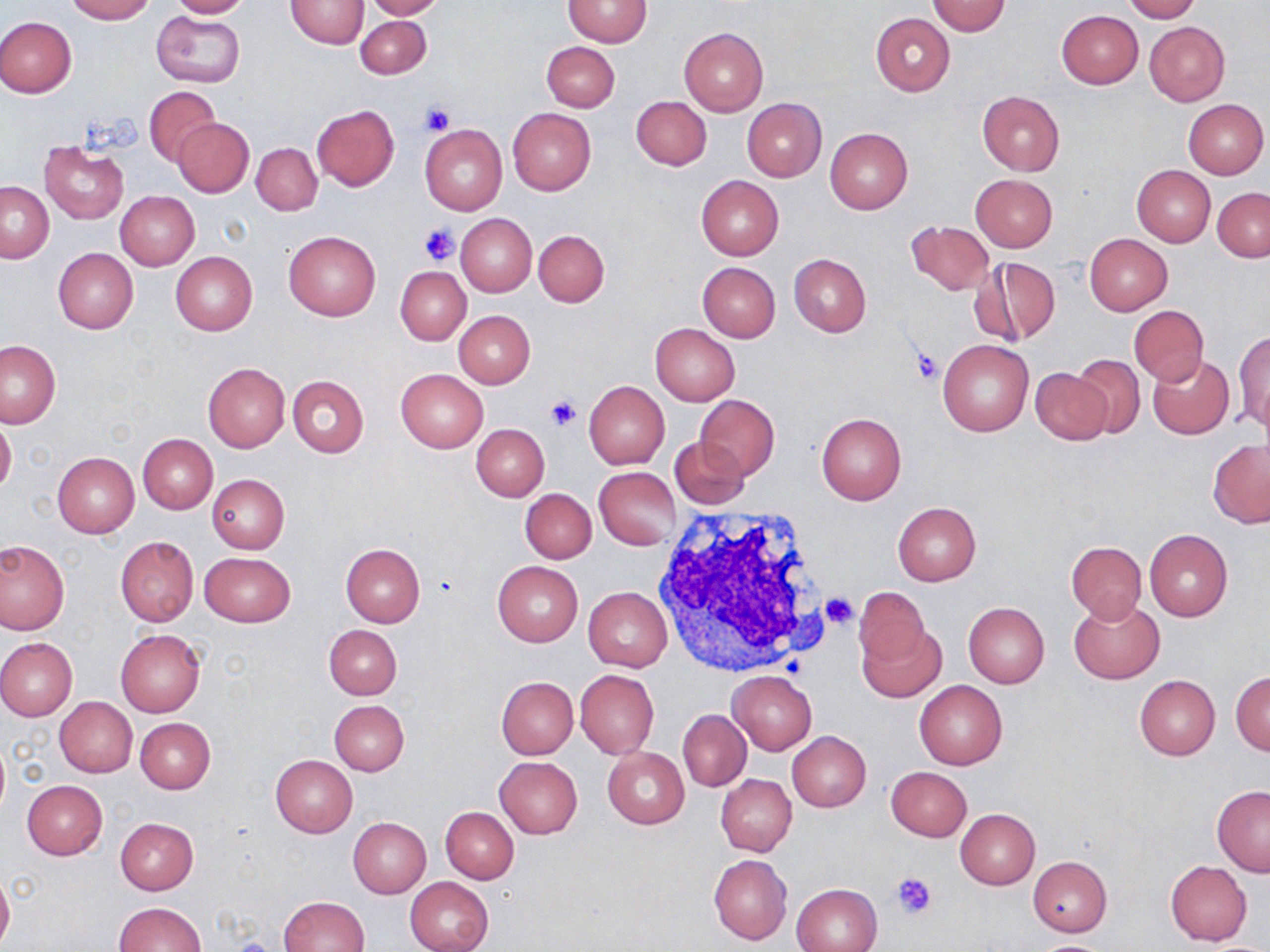

Approximate bounding boxes as [x1, y1, x2, y2] in pixels. Uninfected red blood cell locations: [65, 0, 154, 23], [167, 0, 254, 18], [286, 0, 368, 49], [362, 0, 445, 20], [562, 0, 653, 47], [1122, 0, 1201, 23], [926, 1, 1012, 37], [297, 5, 433, 65], [152, 11, 244, 88], [1055, 11, 1142, 89], [870, 13, 955, 96], [0, 16, 76, 98], [354, 16, 431, 79], [1145, 22, 1229, 105], [679, 27, 768, 116], [541, 41, 620, 112], [144, 88, 222, 167], [976, 90, 1065, 175], [631, 96, 711, 170], [741, 98, 826, 182], [1184, 100, 1268, 179], [312, 104, 399, 191], [508, 109, 595, 195], [174, 118, 253, 197], [420, 123, 507, 215], [825, 128, 913, 214], [39, 141, 129, 224], [252, 143, 322, 215], [1132, 165, 1215, 246], [971, 174, 1057, 252], [696, 175, 783, 260], [1, 182, 54, 262], [1213, 187, 1270, 261], [116, 191, 199, 270], [456, 214, 536, 295], [906, 220, 994, 296], [533, 229, 609, 307], [283, 231, 380, 321], [1084, 234, 1173, 315], [52, 247, 139, 334], [170, 251, 258, 335], [788, 254, 871, 337], [975, 257, 1061, 348], [697, 261, 781, 342], [395, 266, 471, 345], [1129, 307, 1209, 385], [454, 310, 536, 387], [650, 323, 740, 405], [1234, 330, 1270, 433], [938, 339, 1034, 437], [1, 340, 61, 429], [1071, 353, 1145, 438], [1148, 353, 1235, 439], [202, 363, 290, 452], [395, 368, 488, 452], [1030, 368, 1114, 445], [288, 375, 369, 457], [584, 380, 670, 469], [693, 394, 780, 480], [816, 412, 906, 504], [0, 416, 17, 497], [471, 424, 549, 501], [139, 435, 218, 513], [669, 436, 749, 509], [1208, 439, 1269, 527], [52, 452, 140, 538], [594, 467, 681, 549], [208, 474, 290, 553], [520, 488, 596, 564], [892, 501, 981, 584], [1145, 529, 1232, 620], [115, 537, 199, 626], [1, 541, 68, 635], [1067, 541, 1146, 622], [340, 543, 425, 627], [200, 552, 295, 628], [493, 562, 583, 645], [853, 585, 932, 668], [583, 586, 673, 672], [1068, 598, 1166, 684], [963, 601, 1049, 688], [859, 621, 945, 703], [323, 624, 401, 699], [116, 629, 205, 717], [0, 638, 77, 721], [575, 669, 659, 758], [727, 671, 817, 755], [1231, 671, 1270, 755], [1134, 675, 1219, 760], [497, 677, 577, 759], [914, 679, 1008, 769], [55, 696, 138, 777], [328, 699, 410, 777], [679, 710, 750, 790], [136, 718, 215, 793], [787, 731, 871, 812], [0, 738, 10, 817], [601, 746, 689, 828], [271, 755, 357, 836], [494, 756, 583, 838], [885, 766, 972, 841], [716, 774, 797, 856], [22, 781, 107, 859], [1212, 786, 1270, 875], [441, 807, 518, 884], [955, 808, 1039, 889], [115, 817, 198, 895], [348, 817, 431, 898], [708, 854, 792, 945], [1027, 855, 1112, 937], [1164, 860, 1252, 945], [0, 873, 13, 949], [405, 876, 493, 952], [792, 883, 881, 952], [279, 896, 369, 951], [113, 902, 206, 952]. Platelet locations: [421, 103, 455, 137], [420, 223, 460, 266], [911, 348, 942, 384], [546, 395, 579, 431], [819, 591, 859, 629], [892, 873, 938, 919]. White blood cell locations: [648, 506, 836, 678]. Slide-level diagnosis: no evidence of blood parasites. May-Grünwald-Giemsa stain. Thin blood film. 1000x magnification. Single field of view. Light microscopy. Image is 1270×952 pixels.